Assess this cell for malaria.
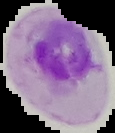

Parasitized.

From a thin blood smear. Segmented cell region on a black background. Image is 115×133 pixels.